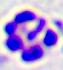

{
  "identification": "leukocyte",
  "modality": "micrograph",
  "magnification": "400x"
}